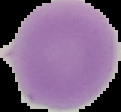
malaria status = uninfected
preparation = thin blood smear
image size = 121×112 pixels
image type = segmented cell region on a black background